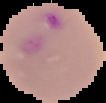
preparation = thin blood smear
malaria status = parasitized
image size = 106×103 pixels
image type = segmented cell region on a black background